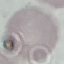

Result: no malaria parasites detected. Photographed with a smartphone camera at the microscope eyepiece. Giemsa-stained preparation. Thin blood film. Automatically extracted cell patch, resized to 64 × 64 pixels.